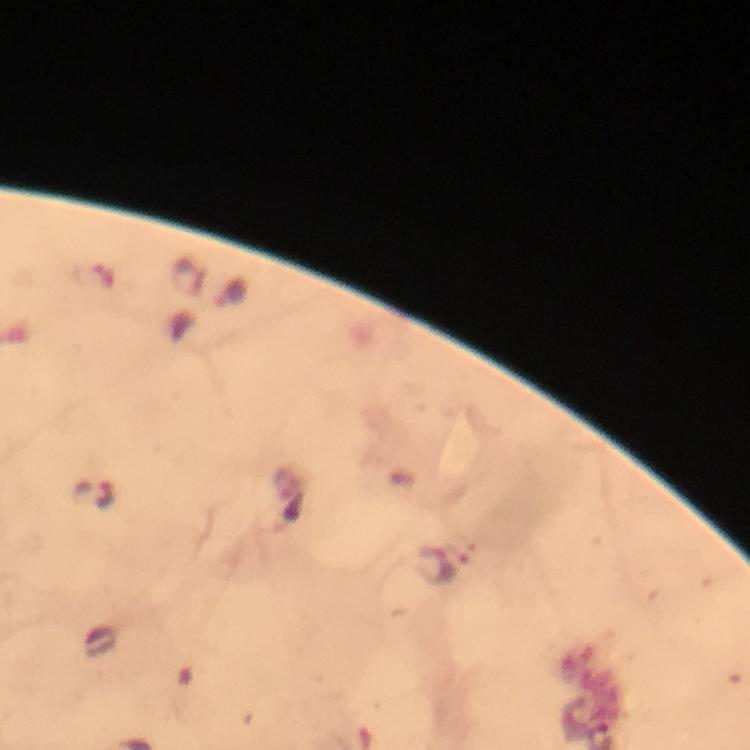 Approximate centers as (x, y) in pixels. Plasmodium parasite locations: (95, 494), (439, 568). At 100x magnification. Image is 750×750 pixels. From a diagnostic examination for malaria. Immersion oil applied. Cropped region of a single field of view. Giemsa-stained preparation. Thick smear. Smartphone photograph taken through a microscope.